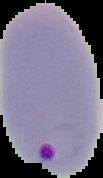 Image is 103×178 pixels. Malaria status: parasitized. From a thin blood smear. Segmented cell region on a black background.